Assess this cell for malaria.
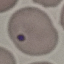

Parasitized.

capture = smartphone camera at the microscope eyepiece
stain = Giemsa
image type = cell patch, automatically extracted from a larger field of view and resized to 64 × 64 pixels
preparation = thin blood film